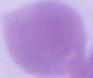

{
  "modality": "photomicrograph",
  "identification": "erythrocyte",
  "magnification": "1000x"
}